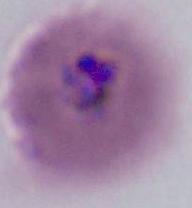

400x or 1000x magnification. A Plasmodium parasite is shown. Photomicrograph.